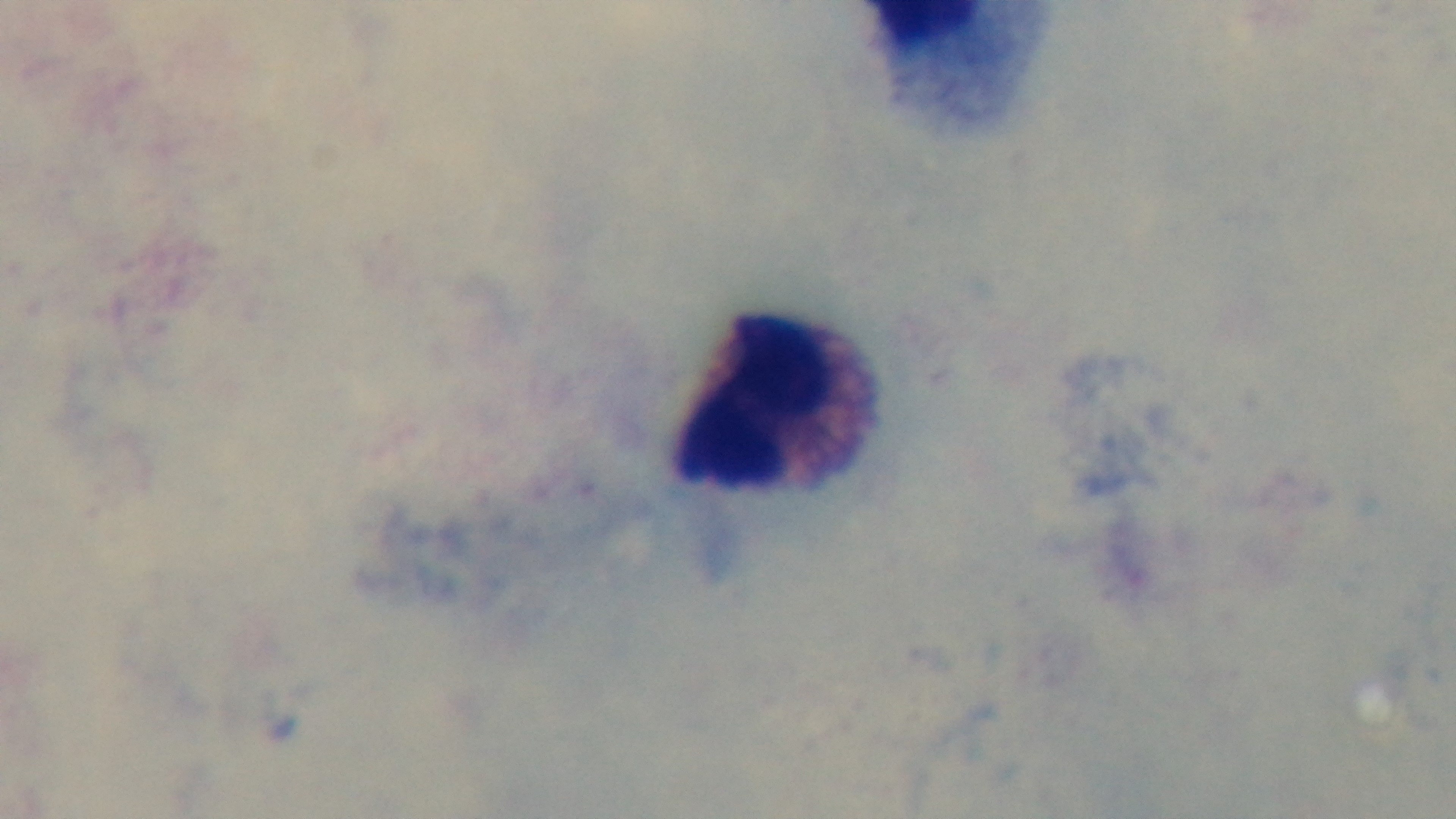

stain = Giemsa
modality = light microscopy
objective = 100x oil immersion
field of view = single
malaria status = uninfected
preparation = thick blood film
capture = mounted 4K digital camera